Classify this cell by malaria status.
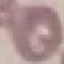

Uninfected.

Summary:
  - Stain: Giemsa
  - Capture: smartphone through the microscope eyepiece
  - Image type: automatically extracted cell patch, resized to 64 × 64 pixels
  - Preparation: thin smear